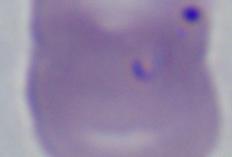

Summary:
  - Magnification: 1000x
  - Identification: Babesia
  - Modality: micrograph